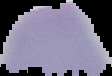
malaria_status: uninfected
image_type: segmented cell region on a black background
image_size: 112×76 pixels
preparation: thin blood smear